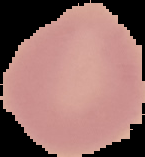

Summary:
  - Image type: segmented cell region on a black background
  - Image size: 145×157 pixels
  - Preparation: thin blood smear
  - Malaria status: uninfected